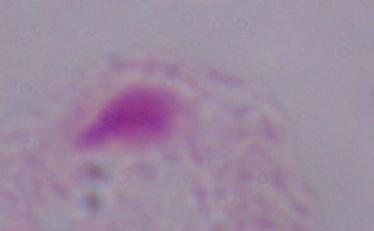
A trichomonad is seen. Photomicrograph. Captured at 1000x magnification.